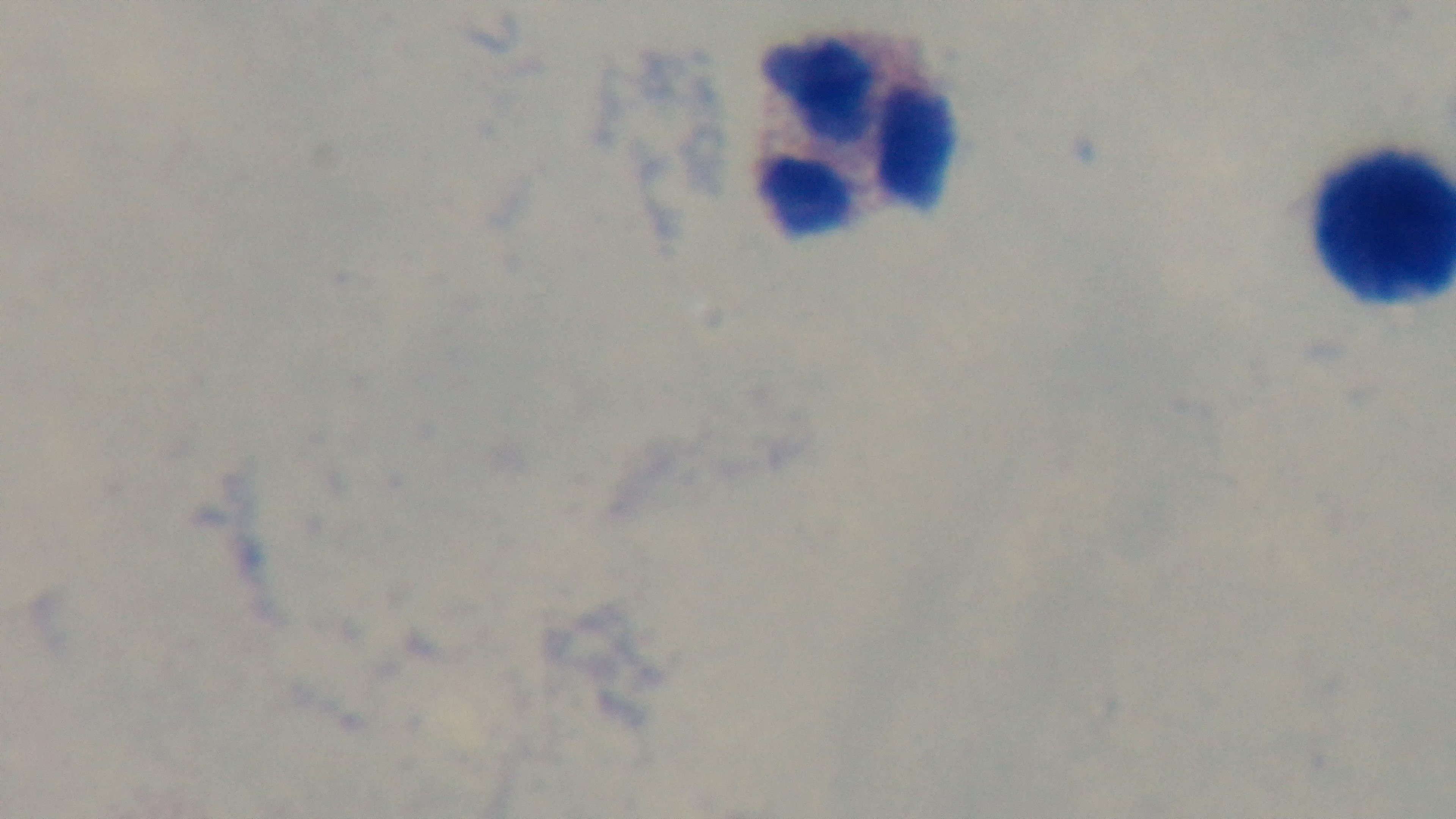

Summary:
  - Preparation: thick
  - Stain: Giemsa
  - Objective: 100x oil immersion
  - Field of view: one from the slide
  - Capture: mounted 4K digital camera
  - Malaria status: uninfected
  - Modality: light microscopy